Report the malaria status of this cell.
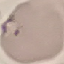
It is parasitized.

Summary:
  - Preparation: thin blood film
  - Image type: automatically extracted cell patch, resized to 64 × 64 pixels
  - Stain: Giemsa
  - Capture: smartphone through the microscope eyepiece